Outline each blood parasite and name the species.
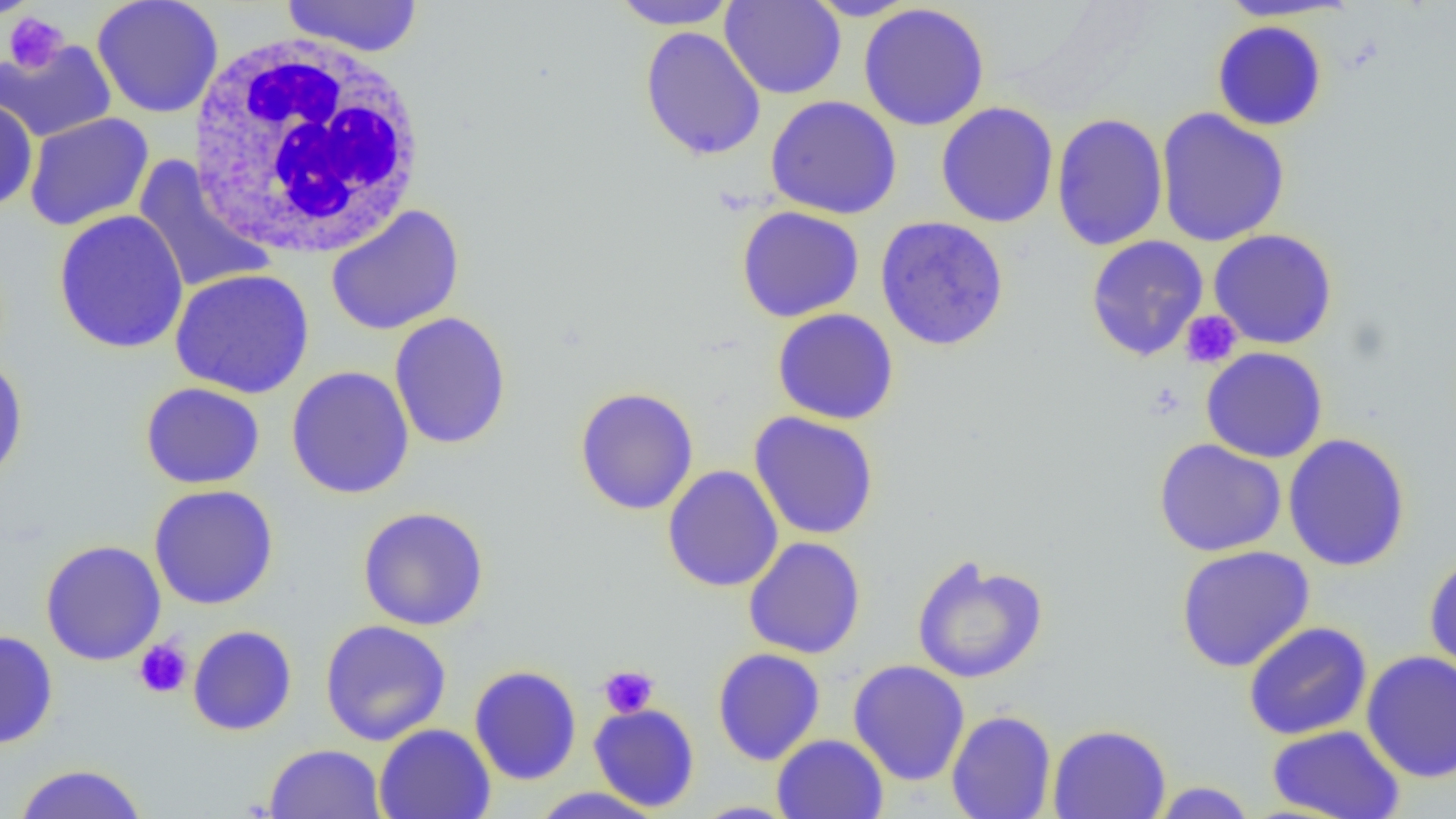
No blood parasites observed.

Approximate bounding boxes as (x1,y1)-(x2,y2) corner pairs in pixels. Uninfected red blood cell locations: (280,0)-(424,58), (719,0)-(846,100), (804,0)-(920,21), (1214,0)-(1357,22), (91,1)-(224,118), (609,1)-(738,30), (858,3)-(990,131), (1211,20)-(1328,131), (639,26)-(766,161), (0,39)-(116,143), (765,94)-(903,219), (0,98)-(38,212), (935,101)-(1059,228), (1155,107)-(1290,247), (24,112)-(154,231), (1051,112)-(1168,251), (131,156)-(277,295), (325,204)-(465,336), (735,205)-(866,322), (52,209)-(189,354), (875,216)-(1009,351), (1208,229)-(1338,350), (1085,235)-(1209,361), (169,268)-(314,399), (772,308)-(899,425), (389,311)-(512,450), (1200,346)-(1328,464), (0,355)-(28,488), (285,365)-(414,499), (140,382)-(266,489), (574,386)-(699,515), (749,411)-(879,540), (1282,433)-(1411,572), (1153,438)-(1287,557), (662,465)-(783,593), (148,484)-(279,610), (357,506)-(489,631), (743,537)-(866,659), (40,540)-(166,666), (1175,545)-(1315,673), (1423,553)-(1456,676), (911,555)-(1049,685), (319,619)-(452,746), (1242,621)-(1373,741), (187,625)-(297,736), (0,630)-(58,749), (712,648)-(825,765), (1361,650)-(1456,783), (848,659)-(970,786), (469,664)-(582,785), (589,703)-(700,811), (946,710)-(1056,819), (373,723)-(496,819), (1047,723)-(1171,819), (1267,725)-(1405,818), (772,734)-(888,819), (263,743)-(386,819), (12,763)-(148,819), (1147,781)-(1258,818), (527,787)-(668,818). White blood cell locations: (186,30)-(429,259). Platelet locations: (2,12)-(69,73), (1180,310)-(1243,369), (133,638)-(193,699), (599,665)-(659,718). Slide-level diagnosis: negative for blood parasites. Optical microscopy. Image is 1456×819 pixels. Captured at 1000x magnification. Thin blood film. Single field of view.